Assess the morphology of the erythrocytes.
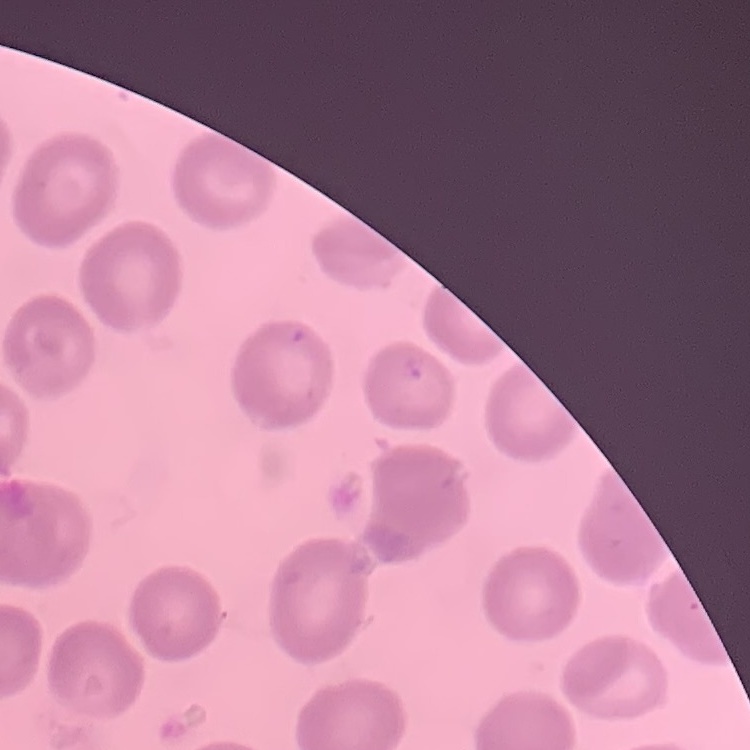
No rouleaux formation.

{
  "preparation": "thin peripheral smear",
  "image_type": "square crop of a larger photomicrograph",
  "stain": "Field's or Giemsa"
}